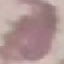
result: negative for malaria parasites
image_type: cell patch, automatically extracted from a larger field of view and resized to 64 × 64 pixels
capture: smartphone camera at the microscope eyepiece
preparation: thin smear
stain: Giemsa